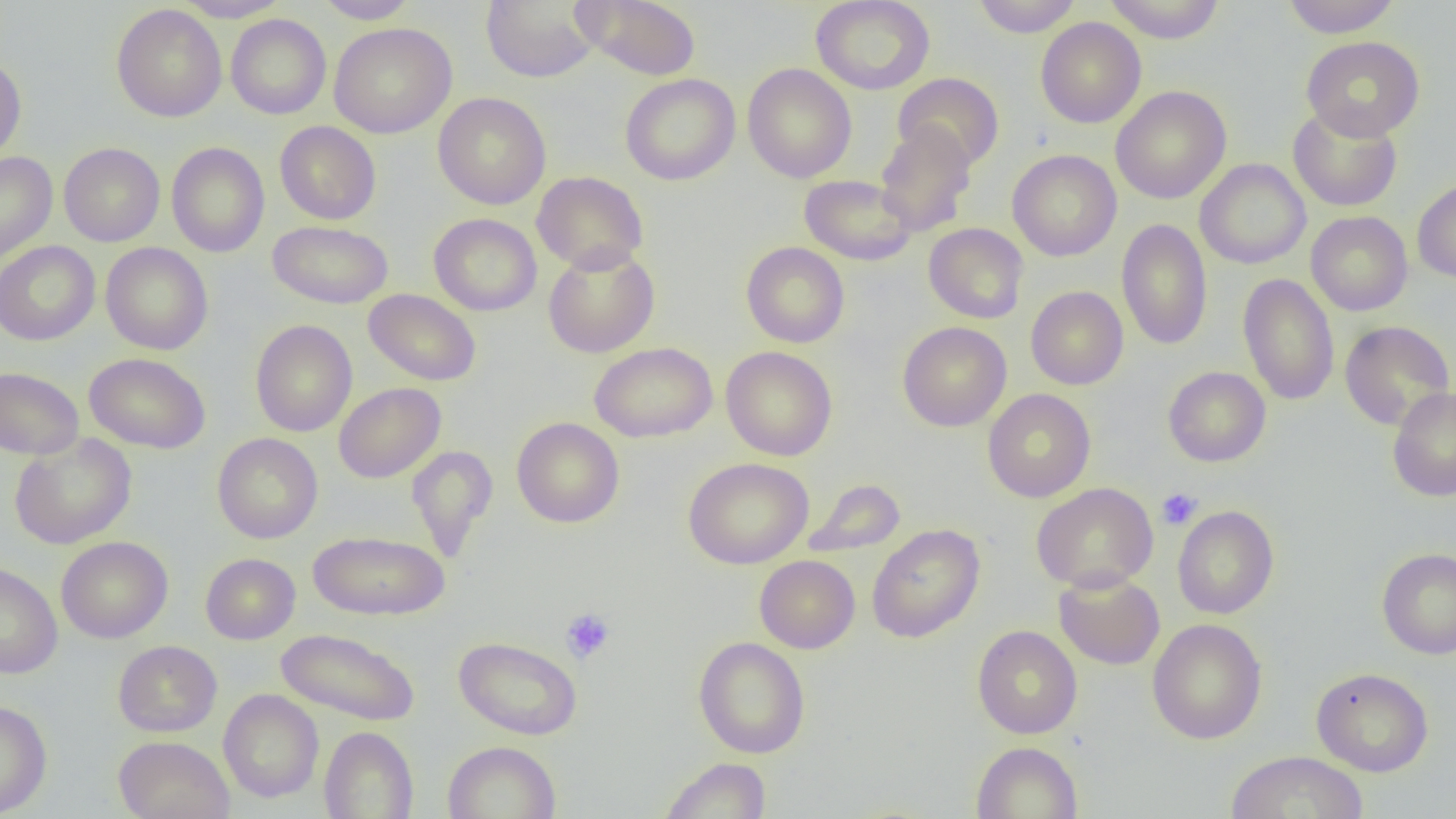
slide-level diagnosis = negative for blood parasites
platelet locations = approximate bounding boxes as named x1/y1/x2/y2 corners in pixels: (x1=1157, y1=488, x2=1202, y2=530), (x1=561, y1=608, x2=616, y2=663)
modality = light microscopy
magnification = 1000x
preparation = thin blood film
uninfected red blood cell locations = approximate bounding boxes as named x1/y1/x2/y2 corners in pixels: (x1=174, y1=0, x2=290, y2=22), (x1=315, y1=0, x2=419, y2=24), (x1=573, y1=0, x2=702, y2=80), (x1=811, y1=0, x2=935, y2=95), (x1=972, y1=0, x2=1082, y2=37), (x1=1103, y1=0, x2=1225, y2=43), (x1=1282, y1=0, x2=1402, y2=38), (x1=481, y1=1, x2=601, y2=83), (x1=111, y1=4, x2=227, y2=122), (x1=225, y1=14, x2=331, y2=119), (x1=1035, y1=17, x2=1146, y2=128), (x1=329, y1=22, x2=456, y2=138), (x1=1301, y1=36, x2=1425, y2=141), (x1=0, y1=56, x2=27, y2=162), (x1=742, y1=63, x2=857, y2=183), (x1=893, y1=72, x2=1004, y2=171), (x1=620, y1=74, x2=740, y2=185), (x1=1110, y1=86, x2=1231, y2=204), (x1=433, y1=92, x2=551, y2=210), (x1=1288, y1=105, x2=1402, y2=212), (x1=275, y1=121, x2=381, y2=225), (x1=875, y1=121, x2=977, y2=236), (x1=167, y1=142, x2=269, y2=257), (x1=58, y1=143, x2=165, y2=247), (x1=1007, y1=149, x2=1122, y2=262), (x1=0, y1=152, x2=58, y2=264), (x1=1195, y1=158, x2=1310, y2=269), (x1=532, y1=171, x2=648, y2=274), (x1=799, y1=174, x2=916, y2=266), (x1=1412, y1=178, x2=1456, y2=283), (x1=1306, y1=211, x2=1412, y2=316), (x1=428, y1=213, x2=542, y2=316), (x1=1116, y1=218, x2=1212, y2=350), (x1=268, y1=220, x2=393, y2=309), (x1=923, y1=223, x2=1028, y2=323), (x1=0, y1=241, x2=100, y2=345), (x1=741, y1=242, x2=850, y2=348), (x1=100, y1=243, x2=213, y2=355), (x1=543, y1=245, x2=659, y2=357), (x1=1238, y1=273, x2=1339, y2=406), (x1=1026, y1=286, x2=1128, y2=390), (x1=364, y1=289, x2=481, y2=386), (x1=250, y1=320, x2=357, y2=437), (x1=1340, y1=320, x2=1454, y2=431), (x1=898, y1=322, x2=1011, y2=431), (x1=589, y1=342, x2=717, y2=443), (x1=721, y1=346, x2=837, y2=461), (x1=85, y1=353, x2=211, y2=453), (x1=1163, y1=366, x2=1271, y2=466), (x1=0, y1=367, x2=83, y2=459), (x1=333, y1=382, x2=446, y2=483), (x1=1387, y1=387, x2=1456, y2=501), (x1=982, y1=388, x2=1096, y2=502), (x1=512, y1=417, x2=625, y2=528), (x1=212, y1=432, x2=323, y2=543), (x1=9, y1=433, x2=137, y2=549), (x1=406, y1=445, x2=498, y2=561), (x1=683, y1=457, x2=813, y2=569), (x1=806, y1=478, x2=906, y2=556), (x1=1031, y1=482, x2=1158, y2=592), (x1=1172, y1=505, x2=1279, y2=619), (x1=867, y1=523, x2=985, y2=643), (x1=308, y1=529, x2=450, y2=621), (x1=56, y1=536, x2=173, y2=643), (x1=1376, y1=548, x2=1456, y2=660), (x1=200, y1=553, x2=300, y2=644), (x1=754, y1=555, x2=860, y2=653), (x1=0, y1=562, x2=63, y2=679), (x1=1054, y1=571, x2=1165, y2=670), (x1=1147, y1=618, x2=1267, y2=744), (x1=972, y1=625, x2=1082, y2=739), (x1=275, y1=628, x2=420, y2=726), (x1=453, y1=636, x2=582, y2=740), (x1=694, y1=636, x2=810, y2=759), (x1=113, y1=640, x2=222, y2=737), (x1=1311, y1=667, x2=1433, y2=777), (x1=219, y1=689, x2=323, y2=802), (x1=0, y1=699, x2=52, y2=817), (x1=319, y1=726, x2=419, y2=818), (x1=113, y1=735, x2=235, y2=819), (x1=442, y1=740, x2=561, y2=819), (x1=971, y1=741, x2=1083, y2=819), (x1=1225, y1=751, x2=1367, y2=818), (x1=659, y1=756, x2=772, y2=818)
field of view = single
image size = 1456×819 pixels